Assess this cell for malaria.
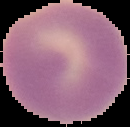
Uninfected.

image size = 130×127 pixels
preparation = thin blood smear
image type = cell region segmented out of the field of view; surrounding area masked to black